Classify this cell by malaria status.
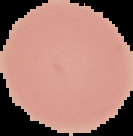
Uninfected.

From a thin blood smear. Segmented cell region on a black background. Image is 133×136 pixels.